Report the malaria status of this cell.
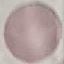

Uninfected.

Giemsa-stained preparation. Photographed with a smartphone camera at the microscope eyepiece. Thin blood smear. Automatically extracted cell patch, resized to 64 × 64 pixels.